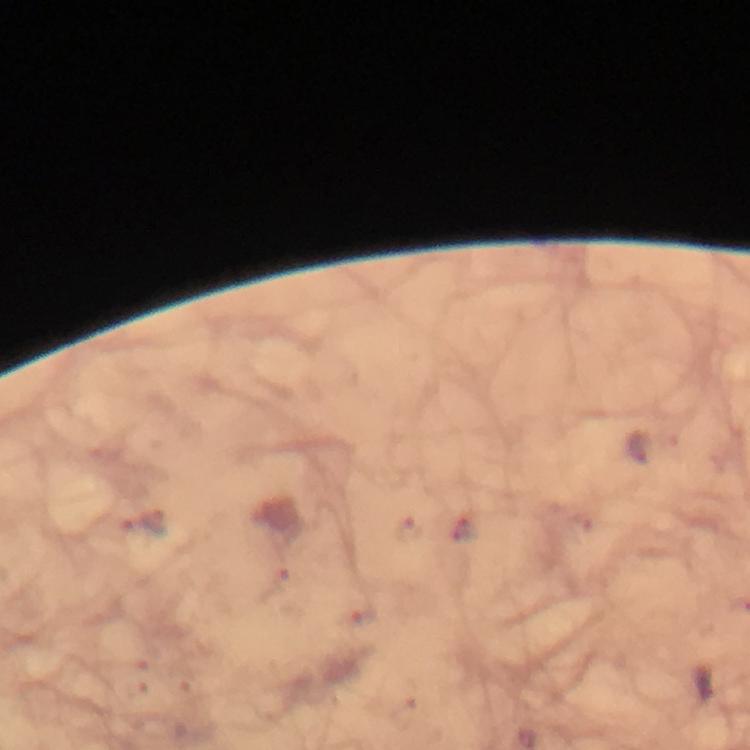

Approximate centers as {x, y} in pixels.
Summary:
  - Plasmodium parasite locations: {142, 524}
  - Context: from a diagnostic examination for malaria
  - Preparation: thick smear
  - Immersion oil: used
  - Capture: smartphone camera through the microscope
  - Image size: 750×750 pixels
  - Magnification: 100x
  - Stain: Giemsa
  - Cropped from: one field of view